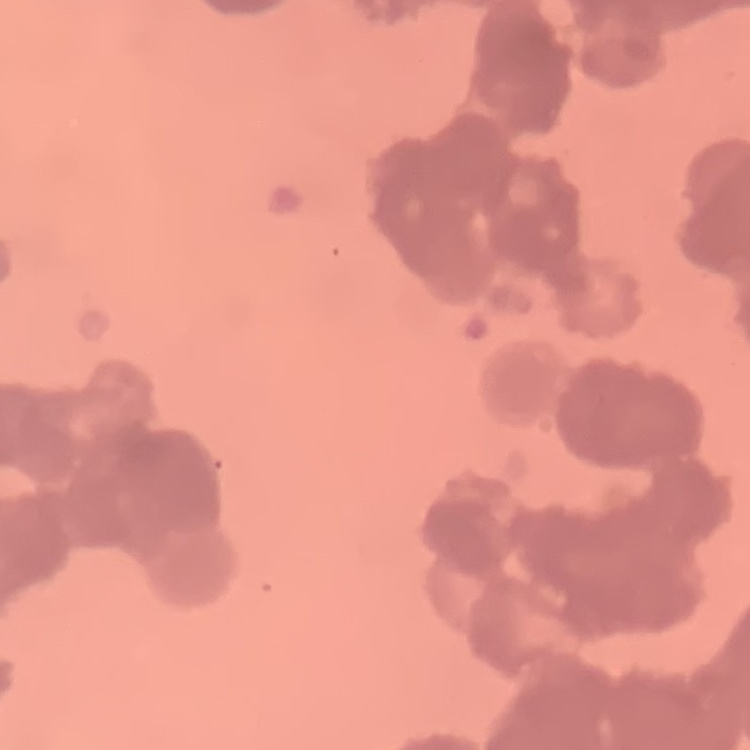

The erythrocytes show rouleaux formation. Field's or Giemsa stain. Square crop of a larger photomicrograph. Thin peripheral smear.